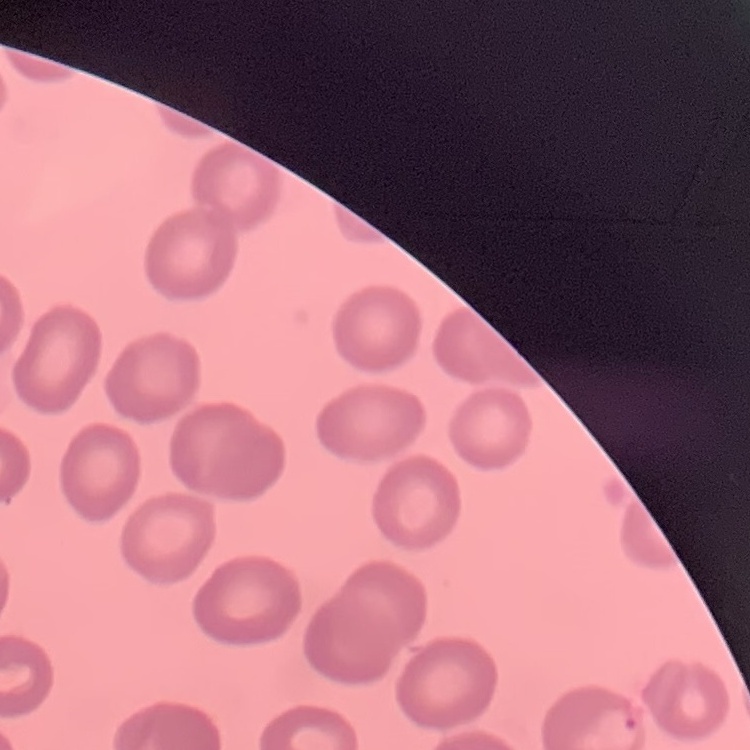
The red blood cells exhibit no rouleaux formation. Thin blood film. Stained with either Field's or Giemsa. Square crop of a larger photomicrograph.